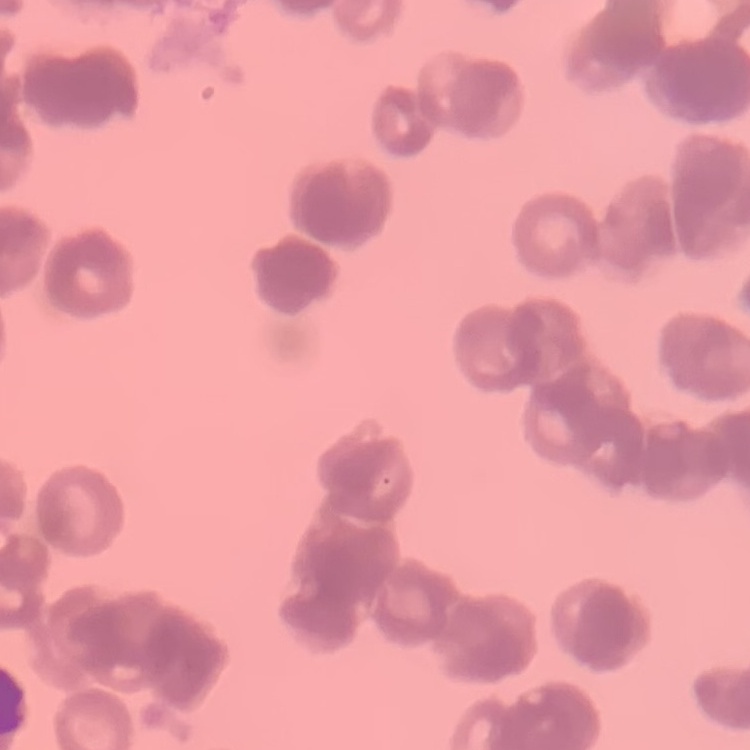

Summary:
  - Erythrocyte morphology: rouleaux formation
  - Preparation: thin blood smear
  - Stain: Field's or Giemsa
  - Image type: square crop of a larger photomicrograph